Evaluate for parasitized red blood cells.
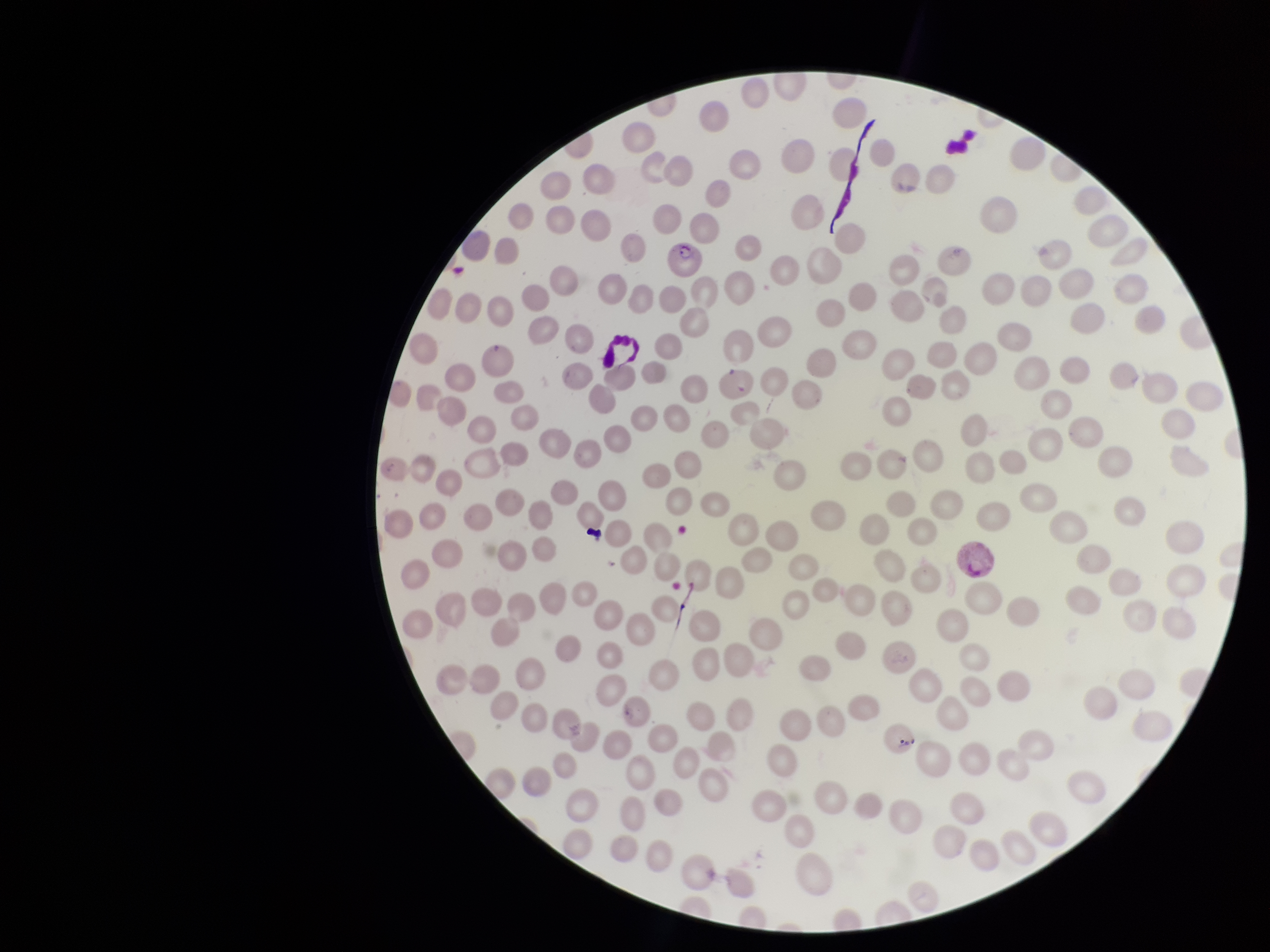

Identified.

stain = Giemsa
capture = smartphone photograph through the microscope eyepiece
patient malaria status = infected
species reported for this patient = Plasmodium vivax
image size = 1270×952 pixels
parasitized red blood cell count = 2
field of view = one from this slide
preparation = thin
red blood cell count = 213